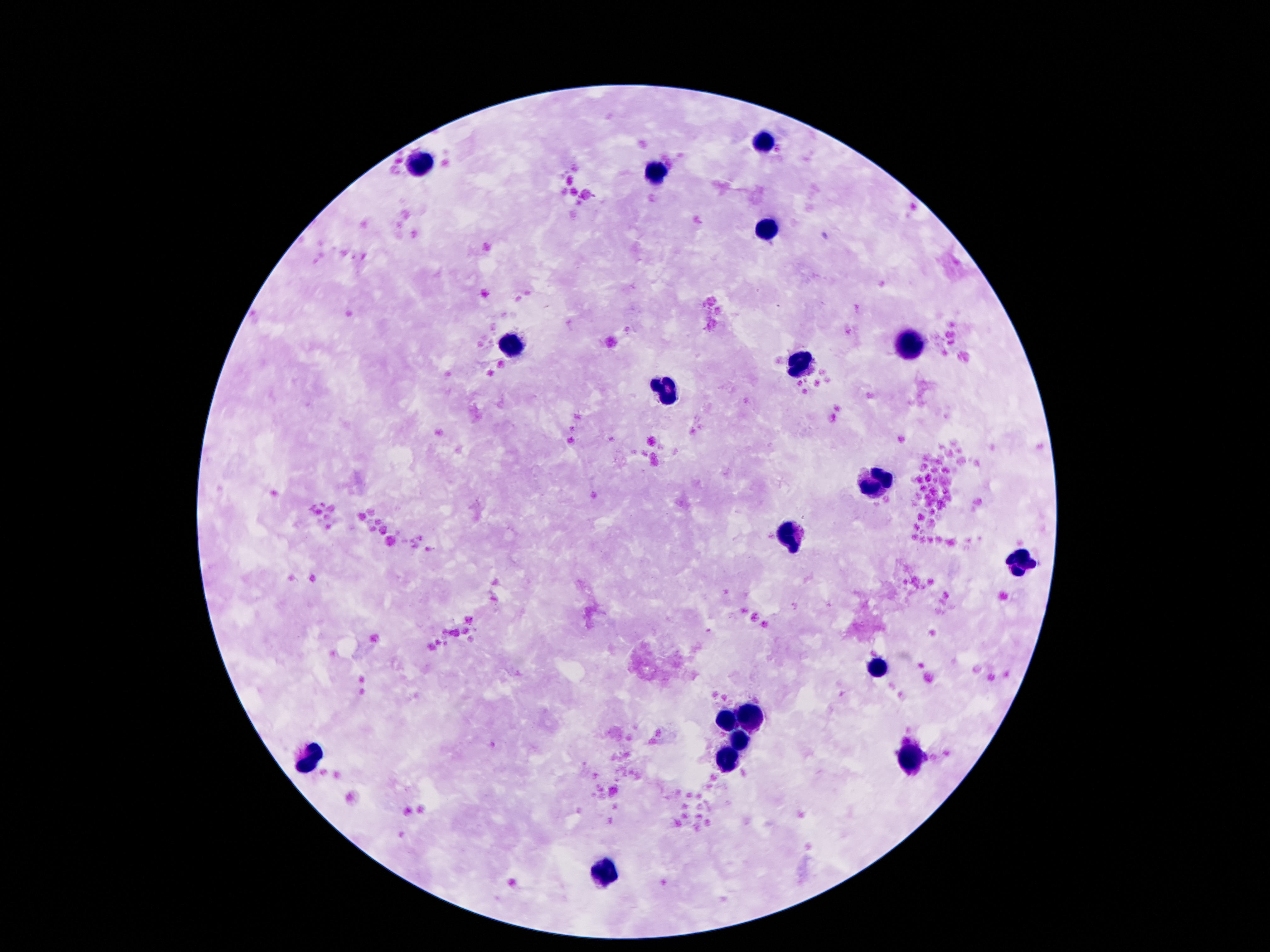
{
  "stain": "Giemsa",
  "capture": "smartphone camera through the microscope eyepiece",
  "field_of_view": "single",
  "leukocyte_locations": "approximate centers as [x, y] in pixels: [767, 137], [418, 162], [653, 175], [769, 228], [910, 344], [513, 346], [805, 366], [670, 388], [874, 484], [790, 537], [1021, 563], [878, 667], [729, 720], [748, 720], [737, 741], [313, 757], [725, 763], [914, 766], [601, 875]",
  "magnification": "100x",
  "patient_malaria_status": "uninfected",
  "preparation": "thick peripheral-blood smear",
  "image_size": "1270×952 pixels"
}